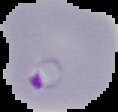
result = malaria parasites detected
image size = 118×112 pixels
preparation = thin blood film
image type = segmented cell region on a black background